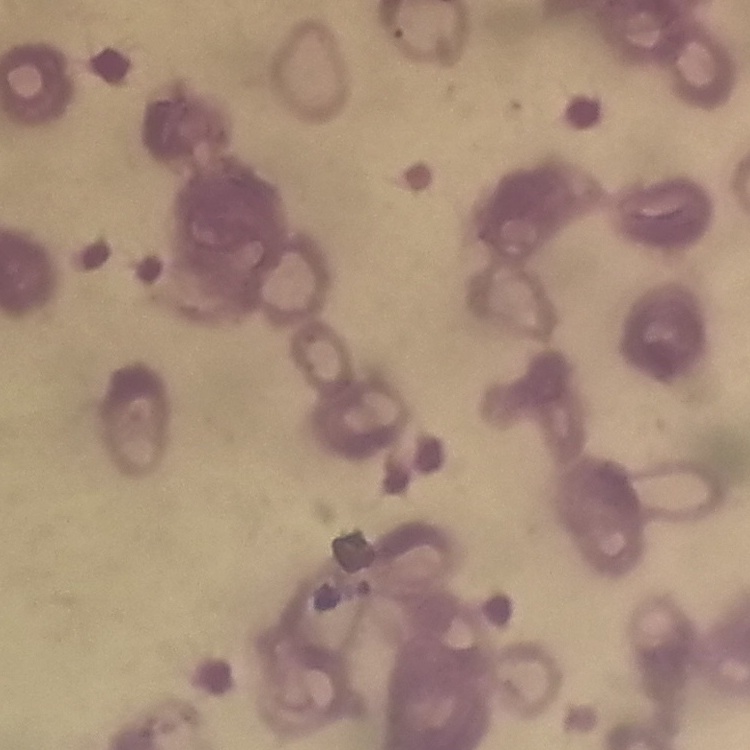

erythrocyte morphology = rouleaux formation
image type = one tile cut from a larger photomicrograph
stain = Field's or Giemsa
preparation = thin blood film